Report the malaria status of this cell.
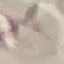
It is uninfected.

Photographed with a smartphone camera at the microscope eyepiece. Giemsa stain. Automatically extracted cell patch, resized to 64 × 64 pixels. Thin blood smear.